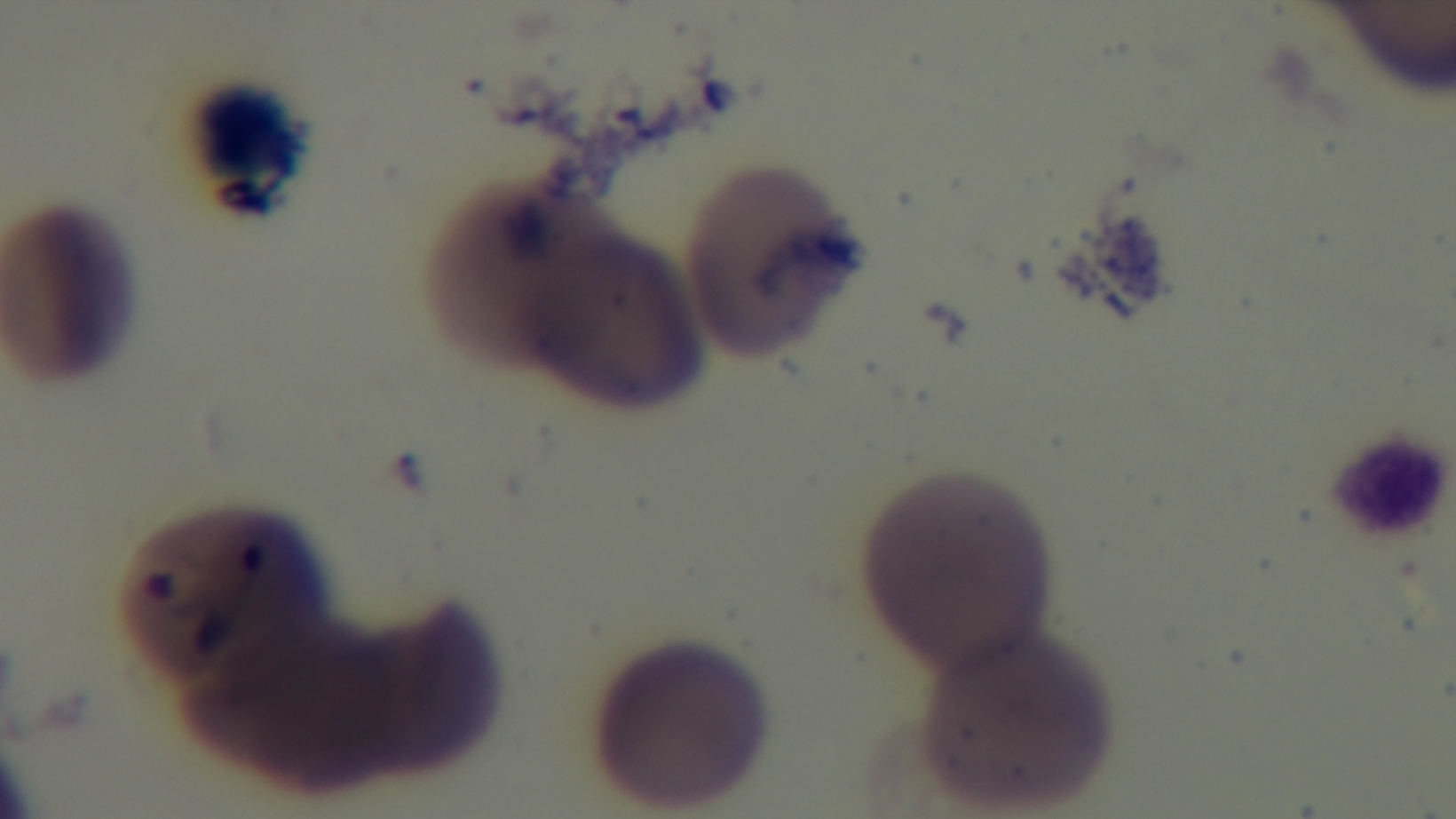
field of view = one from the slide
stain = Giemsa
capture = mounted 4K digital camera
preparation = thin
modality = light microscopy
objective = 100x oil immersion
malaria status = positive